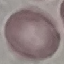
Summary:
  - Result: no malaria parasites detected
  - Capture: smartphone through the microscope eyepiece
  - Stain: Giemsa
  - Image type: cell patch, automatically extracted from a larger field of view and resized to 64 × 64 pixels
  - Preparation: thin blood smear